Locate every Trypanosoma brucei.
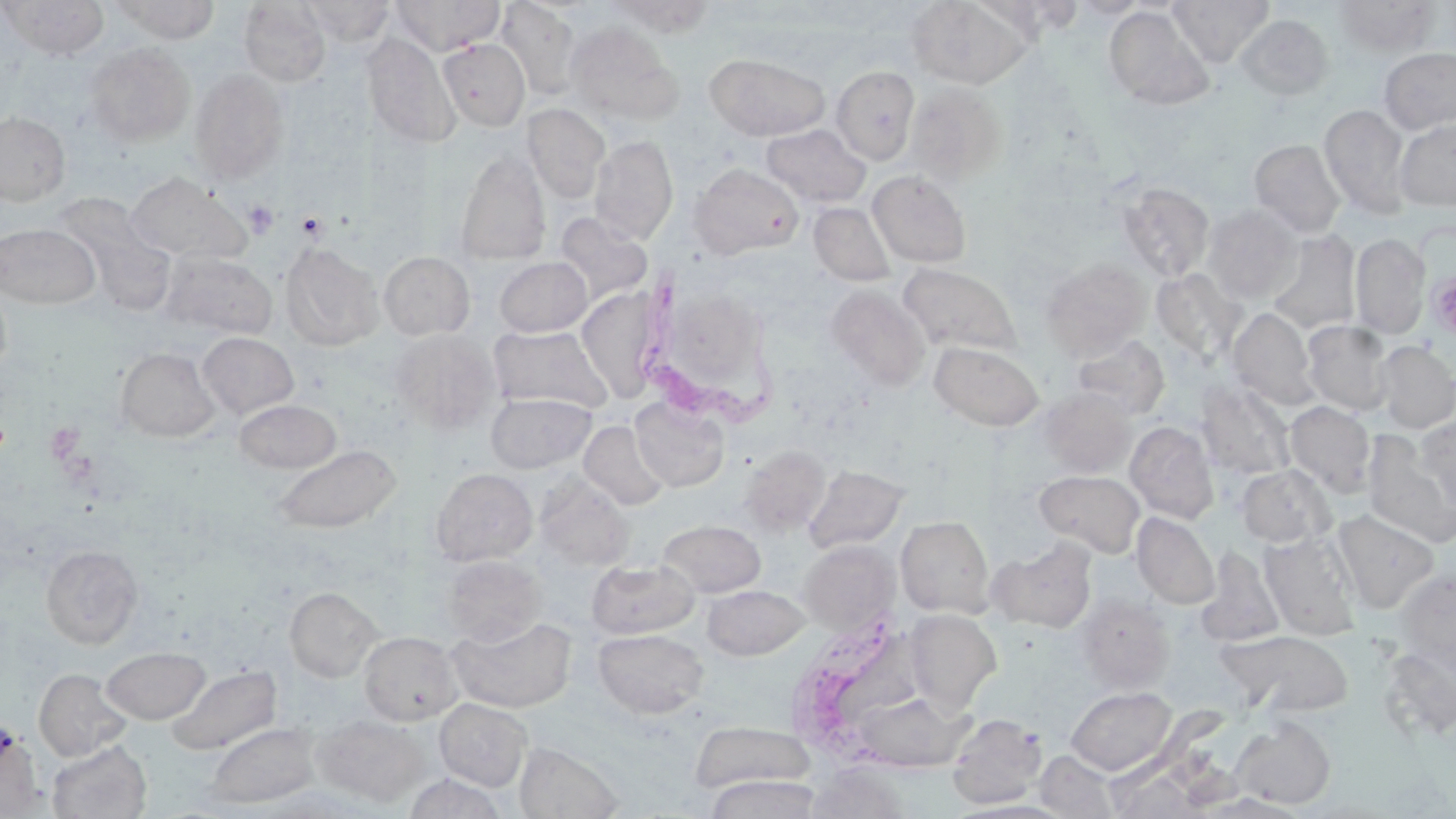
Approximate bounding boxes as (x1,y1)-(x2,y2) corner pairs in pixels.
Trypanosoma brucei: (642,265)-(792,434), (790,609)-(914,767).

slide-level diagnosis = Trypanosoma brucei
uninfected red blood cell locations = approximate bounding boxes as (x1,y1)-(x2,y2) corner pairs in pixels: (2,0)-(110,60), (299,0)-(396,45), (390,0)-(504,56), (494,0)-(583,102), (606,0)-(718,37), (906,0)-(1034,90), (1068,0)-(1149,19), (1168,0)-(1274,67), (1332,0)-(1440,56), (117,1)-(221,44), (238,1)-(331,87), (979,2)-(1092,38), (1104,6)-(1213,109), (1235,14)-(1334,101), (565,21)-(683,125), (361,32)-(460,149), (438,38)-(530,130), (84,43)-(196,146), (1379,47)-(1456,134), (706,53)-(829,141), (831,66)-(921,164), (189,68)-(290,184), (906,80)-(1008,185), (1319,103)-(1412,219), (522,104)-(610,203), (0,112)-(70,205), (1394,117)-(1456,211), (761,123)-(871,208), (590,135)-(679,245), (1250,139)-(1347,237), (455,150)-(551,265), (690,163)-(804,259), (867,170)-(972,268), (124,171)-(250,265), (1118,182)-(1214,282), (44,192)-(162,288), (809,202)-(896,286), (1202,203)-(1302,303), (553,212)-(653,307), (0,223)-(99,308), (1267,231)-(1361,334), (1350,232)-(1431,340), (281,242)-(385,350), (160,251)-(278,341), (379,251)-(475,340), (494,256)-(592,337), (1041,258)-(1151,359), (898,263)-(1020,356), (1151,268)-(1246,364), (0,278)-(12,380), (825,285)-(931,391), (672,289)-(772,387), (583,290)-(664,406), (1228,308)-(1319,410), (1301,320)-(1394,416), (488,325)-(612,413), (391,331)-(498,433), (197,332)-(298,419), (1071,335)-(1170,420), (930,340)-(1044,431), (1374,341)-(1456,433), (115,348)-(220,442), (1195,379)-(1296,480), (1038,388)-(1137,477), (486,392)-(596,474), (630,396)-(730,492), (234,399)-(341,473), (1284,401)-(1376,498), (1414,416)-(1456,514), (579,420)-(669,511), (1125,421)-(1219,524), (1363,433)-(1456,548), (273,444)-(401,533), (740,444)-(830,536), (803,465)-(908,554), (1236,465)-(1334,548), (430,468)-(538,566), (1035,469)-(1145,557), (535,475)-(633,570), (1332,509)-(1440,612), (1132,513)-(1219,609), (896,515)-(995,617), (658,519)-(766,597), (1259,530)-(1360,639), (988,537)-(1098,633), (798,540)-(899,634), (40,545)-(143,649), (1196,547)-(1285,646), (443,555)-(546,646), (586,558)-(699,639), (1395,571)-(1456,667), (702,585)-(809,660), (285,587)-(382,682), (1075,594)-(1174,692), (904,609)-(1002,713), (448,616)-(577,713), (592,629)-(708,719), (1220,630)-(1356,716), (359,631)-(462,725), (1377,642)-(1456,747), (101,646)-(209,724), (167,664)-(282,755), (34,668)-(132,761), (1066,686)-(1177,775), (848,689)-(972,772), (435,699)-(532,791), (947,712)-(1047,809), (312,715)-(430,806), (1230,716)-(1336,809), (688,719)-(816,796), (206,723)-(319,808), (47,740)-(152,819), (514,741)-(624,818), (1034,749)-(1121,818), (1104,762)-(1217,816), (805,765)-(912,818), (403,773)-(506,818), (704,774)-(822,818)
platelet locations = approximate bounding boxes as (x1,y1)-(x2,y2) corner pairs in pixels: (243,200)-(279,239), (295,211)-(328,241), (1427,271)-(1456,341)
image size = 1456×819 pixels
field of view = one of a larger specimen
modality = optical microscopy
stain = May-Grünwald-Giemsa
preparation = thin blood smear
magnification = 1000x